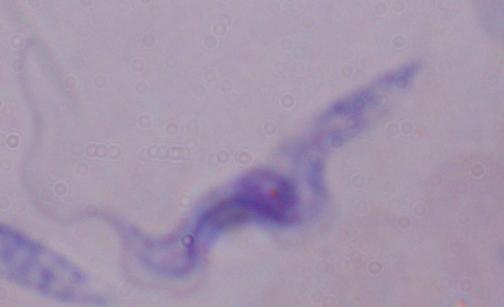

identification: trypanosome
magnification: 1000x
modality: micrograph